Report the malaria status of this cell.
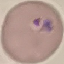

It is parasitized.

Summary:
  - Image type: cell patch, automatically extracted from a larger field of view and resized to 64 × 64 pixels
  - Stain: Giemsa
  - Preparation: thin blood film
  - Capture: smartphone camera at the microscope eyepiece